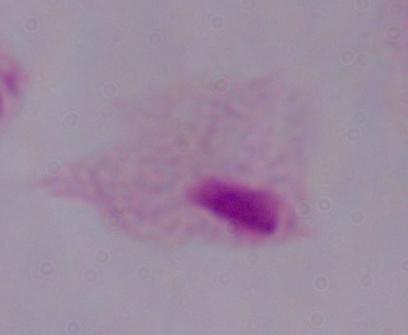

Summary:
  - Magnification: 1000x
  - Identification: trichomonad
  - Modality: micrograph